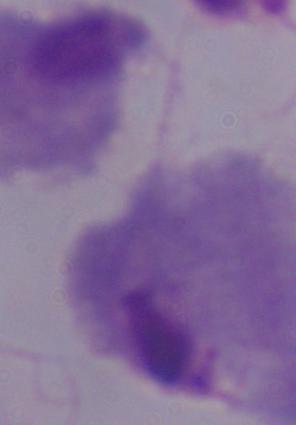
Captured at 1000x magnification. Micrograph. A trichomonad is shown.